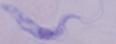 Photomicrograph. 1000x magnification. A trypanosome is shown.